Identify the blood parasite species.
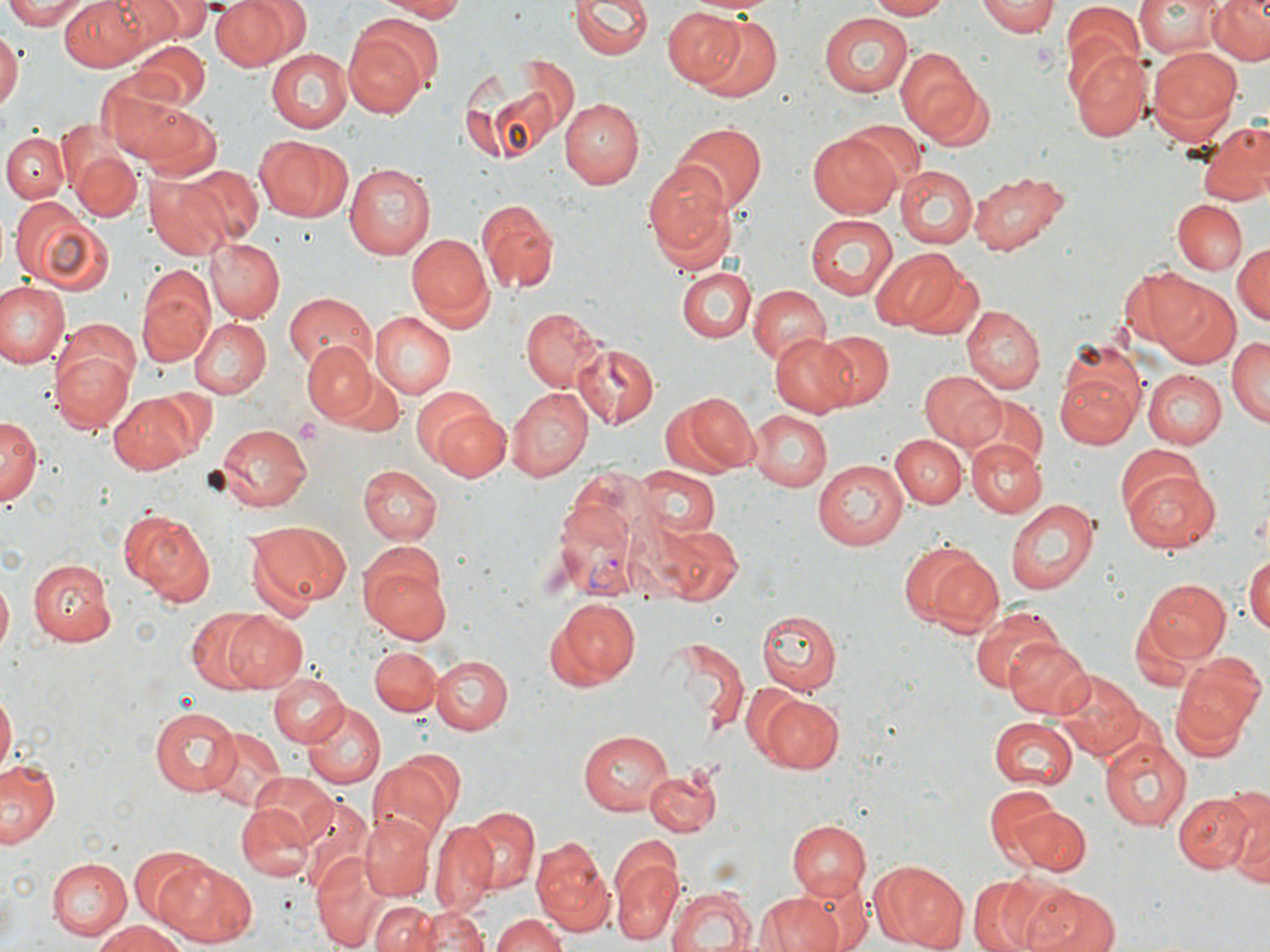

Plasmodium vivax.

Approximate bounding boxes as (x1, y1, x2, y2) in pixels. Platelet locations: (292, 417, 321, 446). Plasmodium vivax-infected red blood cell locations: (551, 498, 642, 600). Uninfected red blood cell locations: (3, 0, 92, 27), (59, 0, 152, 70), (113, 0, 205, 41), (211, 0, 299, 72), (374, 0, 469, 21), (562, 0, 733, 66), (571, 0, 652, 60), (867, 0, 952, 20), (976, 0, 1057, 38), (1135, 0, 1224, 57), (1205, 0, 1270, 66), (1060, 1, 1143, 92), (662, 5, 747, 88), (688, 12, 785, 105), (820, 14, 912, 98), (343, 19, 438, 117), (0, 32, 20, 114), (130, 39, 210, 109), (1146, 45, 1244, 145), (895, 47, 991, 149), (1070, 47, 1152, 141), (266, 48, 354, 134), (101, 75, 206, 166), (472, 81, 563, 168), (127, 99, 224, 179), (559, 99, 644, 189), (843, 120, 925, 199), (1194, 122, 1270, 206), (675, 124, 765, 218), (3, 133, 70, 203), (806, 133, 902, 218), (258, 136, 353, 223), (71, 150, 141, 220), (644, 161, 737, 262), (342, 164, 434, 260), (180, 165, 262, 244), (896, 167, 978, 248), (968, 168, 1068, 255), (143, 170, 235, 259), (6, 195, 116, 299), (1173, 200, 1248, 275), (477, 202, 557, 294), (805, 213, 897, 300), (407, 233, 493, 325), (204, 238, 285, 323), (1232, 239, 1269, 329), (870, 249, 964, 331), (136, 263, 217, 367), (1118, 265, 1216, 355), (904, 267, 985, 342), (678, 269, 754, 343), (0, 280, 68, 371), (747, 283, 829, 364), (1157, 284, 1240, 369), (283, 292, 377, 373), (962, 305, 1045, 394), (519, 307, 608, 392), (371, 309, 458, 399), (379, 310, 482, 458), (188, 317, 271, 398), (815, 330, 896, 408), (771, 335, 859, 417), (1227, 337, 1269, 427), (573, 341, 660, 429), (302, 342, 376, 419), (51, 346, 137, 431), (1056, 365, 1145, 449), (337, 368, 406, 440), (1141, 369, 1225, 448), (918, 370, 1005, 449), (504, 389, 590, 482), (681, 389, 810, 489), (664, 391, 757, 476), (107, 392, 203, 473), (967, 396, 1048, 476), (426, 405, 511, 482), (746, 408, 832, 491), (0, 412, 40, 506), (212, 422, 311, 512), (889, 433, 967, 507), (967, 440, 1047, 519), (1117, 443, 1207, 522), (814, 459, 909, 549), (1121, 465, 1220, 554), (360, 466, 441, 544), (633, 466, 718, 537), (1005, 499, 1099, 596), (120, 509, 214, 607), (243, 518, 349, 615), (661, 525, 742, 606), (897, 541, 999, 635), (359, 551, 454, 644), (1245, 555, 1270, 641), (27, 557, 116, 643), (0, 573, 12, 660), (1137, 578, 1232, 662), (546, 598, 640, 691), (968, 604, 1063, 693), (185, 608, 269, 692), (755, 608, 844, 696), (220, 612, 306, 692), (1004, 637, 1094, 719), (664, 638, 750, 734), (369, 645, 442, 715), (431, 655, 513, 735), (1169, 657, 1264, 751), (1055, 673, 1146, 760), (267, 674, 349, 748), (0, 691, 17, 776), (758, 692, 843, 772), (302, 702, 383, 786), (149, 708, 239, 797), (989, 717, 1078, 789), (203, 727, 287, 813), (579, 729, 672, 815), (1101, 737, 1191, 830), (1, 757, 62, 848), (368, 762, 454, 851), (644, 765, 722, 835), (248, 771, 339, 850), (1225, 782, 1269, 886), (984, 786, 1067, 874), (1172, 790, 1256, 871), (294, 794, 372, 891), (237, 804, 315, 884), (1009, 805, 1091, 877), (460, 806, 540, 894), (359, 815, 435, 898), (785, 819, 873, 897), (430, 821, 497, 913), (533, 836, 612, 932), (128, 847, 211, 925), (310, 849, 389, 949), (612, 849, 682, 946), (47, 856, 132, 940), (154, 859, 257, 947), (867, 862, 967, 951), (784, 870, 871, 952), (972, 873, 1082, 952), (1021, 883, 1121, 952), (667, 886, 756, 952), (755, 889, 849, 952), (371, 900, 440, 952), (419, 906, 489, 952), (492, 913, 570, 952), (95, 919, 190, 952). May-Grünwald-Giemsa-stained preparation. Captured at 1000x magnification. Single field of view. Thin blood smear. Image is 1270×952 pixels. Light microscopy.